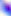
modality = photomicrograph
identification = Toxoplasma gondii
magnification = 400x